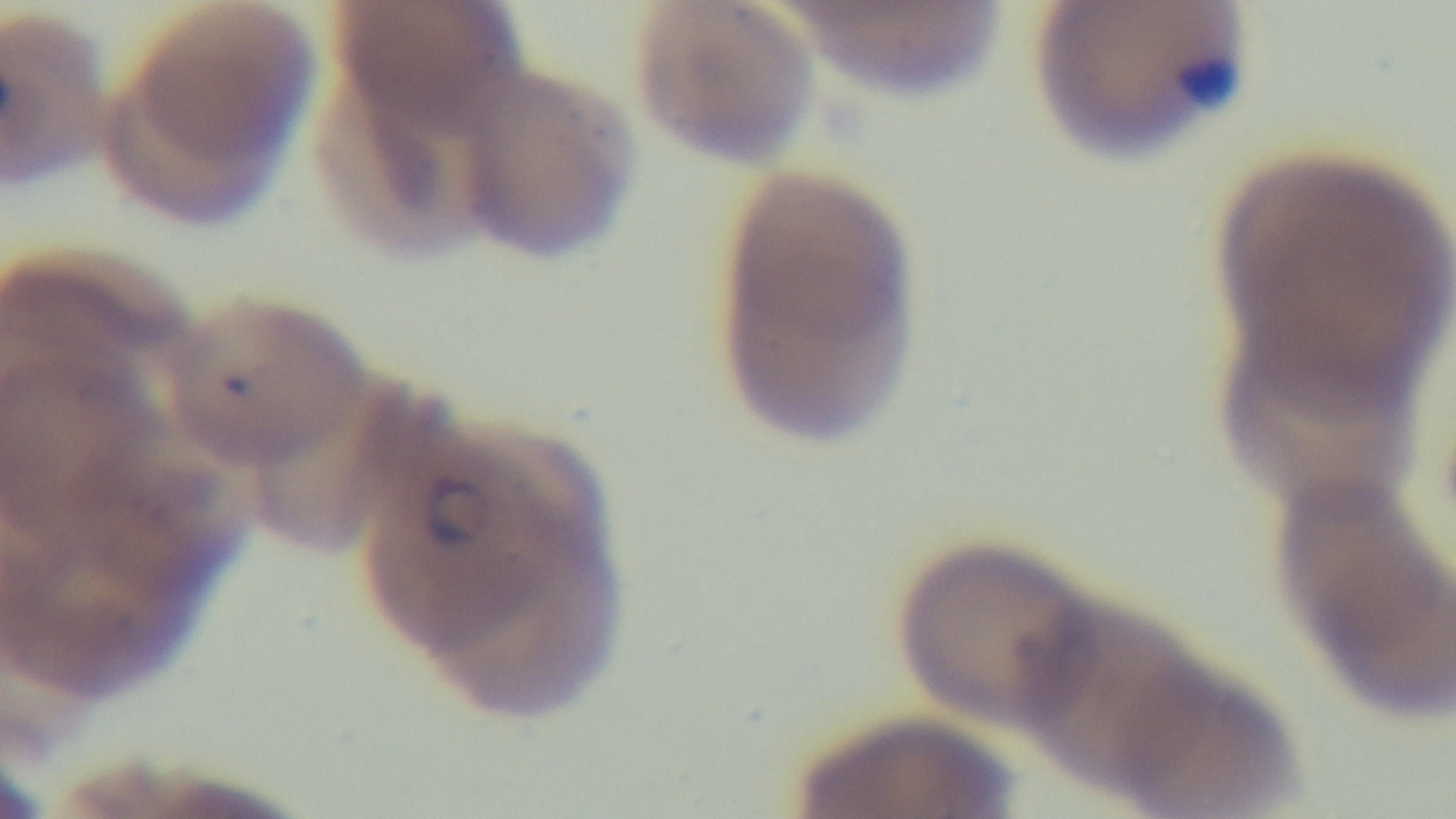
objective = 100x oil immersion
modality = light microscopy
stain = Giemsa
malaria status = positive
preparation = thin smear
capture = mounted 4K digital camera
field of view = one from the slide